Point out each leukocyte.
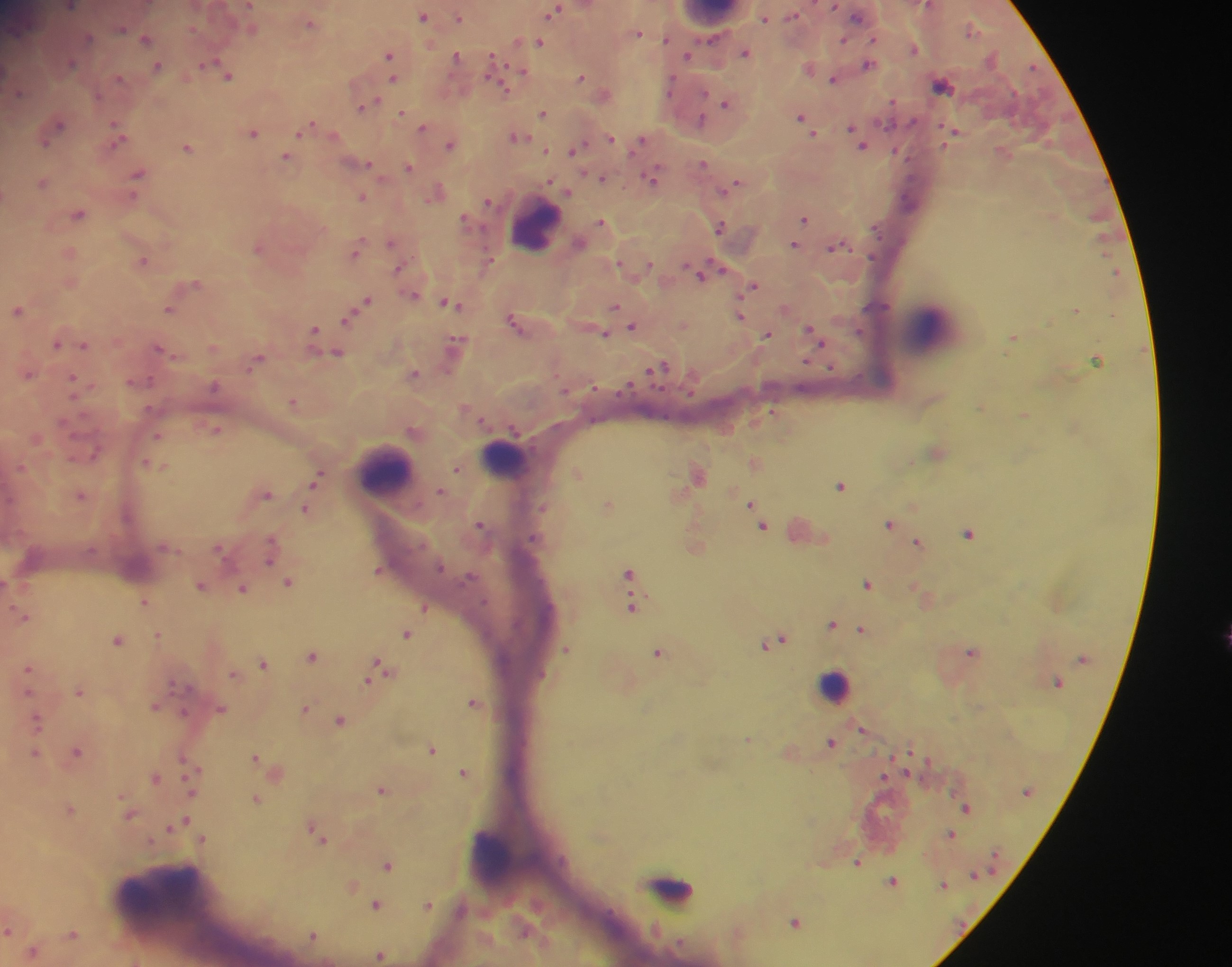
Approximate centers as x y in pixels.
Leukocytes: 712 16; 535 226; 932 328; 504 458; 386 471; 834 686; 882 819; 492 854; 671 888; 170 906.

Malaria parasite locations: 929 5; 70 7; 837 7; 555 10; 798 14; 424 16; 459 17; 765 18; 311 22; 973 30; 639 32; 146 39; 849 41; 539 42; 874 43; 915 49; 745 52; 490 53; 688 56; 458 57; 390 58; 70 63; 869 64; 158 66; 506 66; 1032 67; 810 69; 392 71; 522 71; 228 75; 674 76; 487 78; 582 78; 120 79; 394 79; 834 80; 942 85; 503 87; 605 94; 705 94; 670 96; 727 103; 365 106; 544 113; 402 114; 802 118; 917 118; 424 127; 54 128; 312 128; 955 131; 253 132; 119 136; 816 136; 518 137; 859 137; 611 139; 640 142; 452 144; 188 147; 577 149; 894 150; 1003 152; 287 157; 909 157; 704 164; 370 167; 409 167; 139 174; 601 177; 654 178; 44 182; 733 185; 436 193; 362 196; 903 197; 489 200; 78 214; 805 217; 467 220; 602 222; 721 226; 874 226; 393 242; 795 245; 837 245; 260 246; 356 251; 70 253; 875 256; 143 261; 650 264; 615 265; 724 269; 703 273; 192 285; 754 286; 413 295; 366 301; 451 304; 616 306; 170 308; 18 309; 1077 309; 741 314; 350 317; 517 324; 634 327; 812 331; 603 332; 858 332; 768 335; 319 337; 1013 338; 58 343; 84 344; 455 346; 164 351; 334 352; 258 359; 1098 359; 807 362; 660 368; 831 369; 28 373; 414 373; 140 380; 213 381; 74 382; 591 382; 630 388; 617 391; 567 394; 687 395; 293 402; 469 407; 774 412; 1024 415; 672 419; 510 428; 215 429; 414 431; 35 438; 937 451; 755 461; 154 464; 457 469; 578 473; 698 474; 317 477; 842 485; 441 491; 265 492; 81 494; 609 504; 751 504; 544 508; 306 509; 890 523; 481 524; 763 524; 806 530; 969 533; 533 539; 919 542; 272 547; 379 570; 447 570; 630 572; 477 575; 290 582; 868 583; 202 585; 244 588; 924 594; 145 602; 487 604; 633 605; 425 607; 23 615; 833 624; 861 629; 407 633; 159 634; 119 639; 778 639; 568 648; 659 651; 972 651; 313 655; 264 663; 380 668; 29 671; 234 674; 544 675; 80 690; 474 701; 156 705; 306 707; 221 708; 38 721; 341 721; 864 729; 749 740; 832 741; 432 749; 909 750; 77 751; 35 753; 929 757; 257 759; 275 770; 465 770; 908 772; 192 776; 884 776; 155 777; 383 788; 1025 792; 257 798; 966 808; 71 810; 130 814; 187 820; 177 825; 317 830; 951 834; 202 838; 995 853; 561 859; 858 862; 388 863; 991 869; 975 877; 893 880; 944 885; 352 886; 377 904; 428 904; 610 913; 796 922; 9 929; 73 933; 313 934; 675 942; 34 951; 381 954. Photographed through a microscope with a mobile-phone camera. Image is 1232×967 pixels. Sample from Ghana. One field of view. Thick blood film.